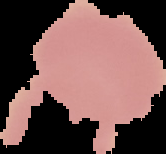

Segmented cell region on a black background. Malaria status: uninfected. From a thin blood smear. Image is 166×154 pixels.